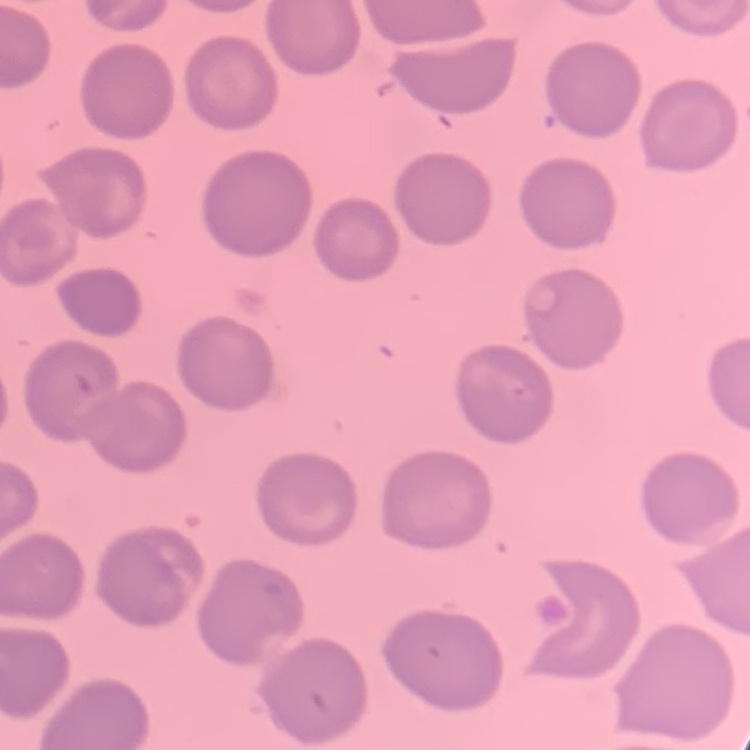
Summary:
  - Red blood cell morphology: no rouleaux formation
  - Image type: one tile cut from a larger photomicrograph
  - Stain: Field's or Giemsa
  - Preparation: thin blood film